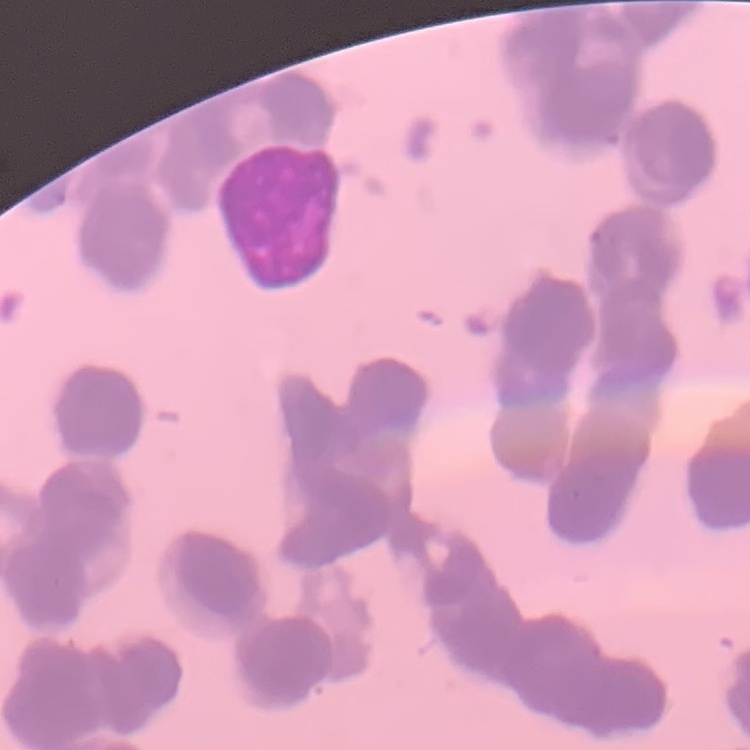 The red blood cells show rouleaux formation. One tile cut from a larger photomicrograph. Field's or Giemsa stain. Thin peripheral smear.